Comment on the morphology of the erythrocytes.
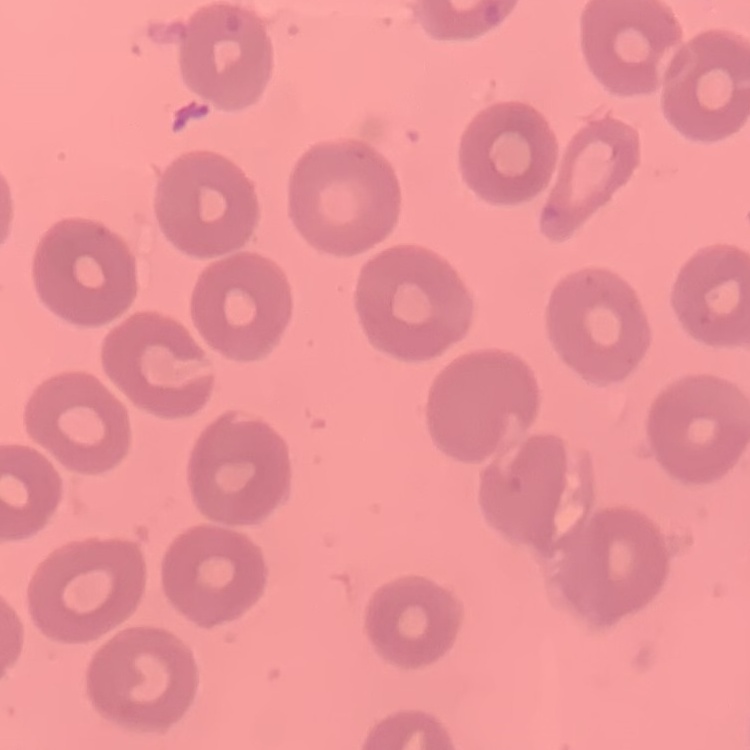

They show no rouleaux formation.

image_type: one tile cut from a larger photomicrograph
preparation: thin blood smear
stain: Field's or Giemsa